Name the parasite shown.
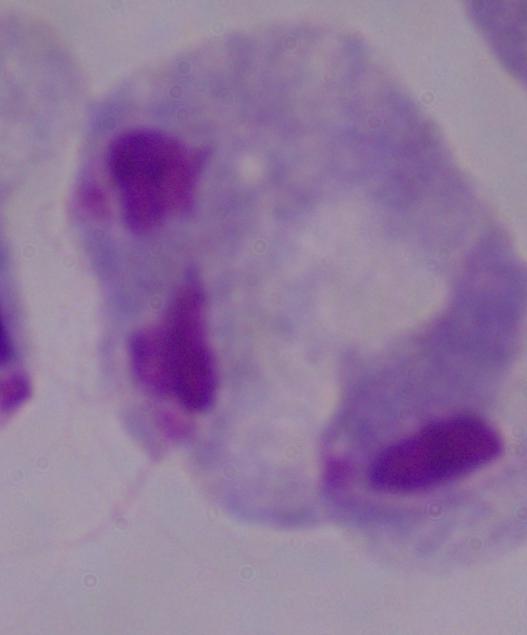

A trichomonad.

1000x magnification. Micrograph.